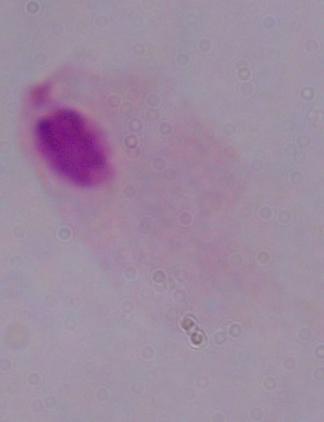
Summary:
  - Modality: photomicrograph
  - Magnification: 1000x
  - Identification: trichomonad